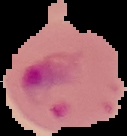

Summary:
  - Preparation: thin blood smear
  - Image size: 127×136 pixels
  - Malaria status: parasitized
  - Image type: cell region segmented out of the field of view; surrounding area masked to black